Evaluate for parasitized red blood cells.
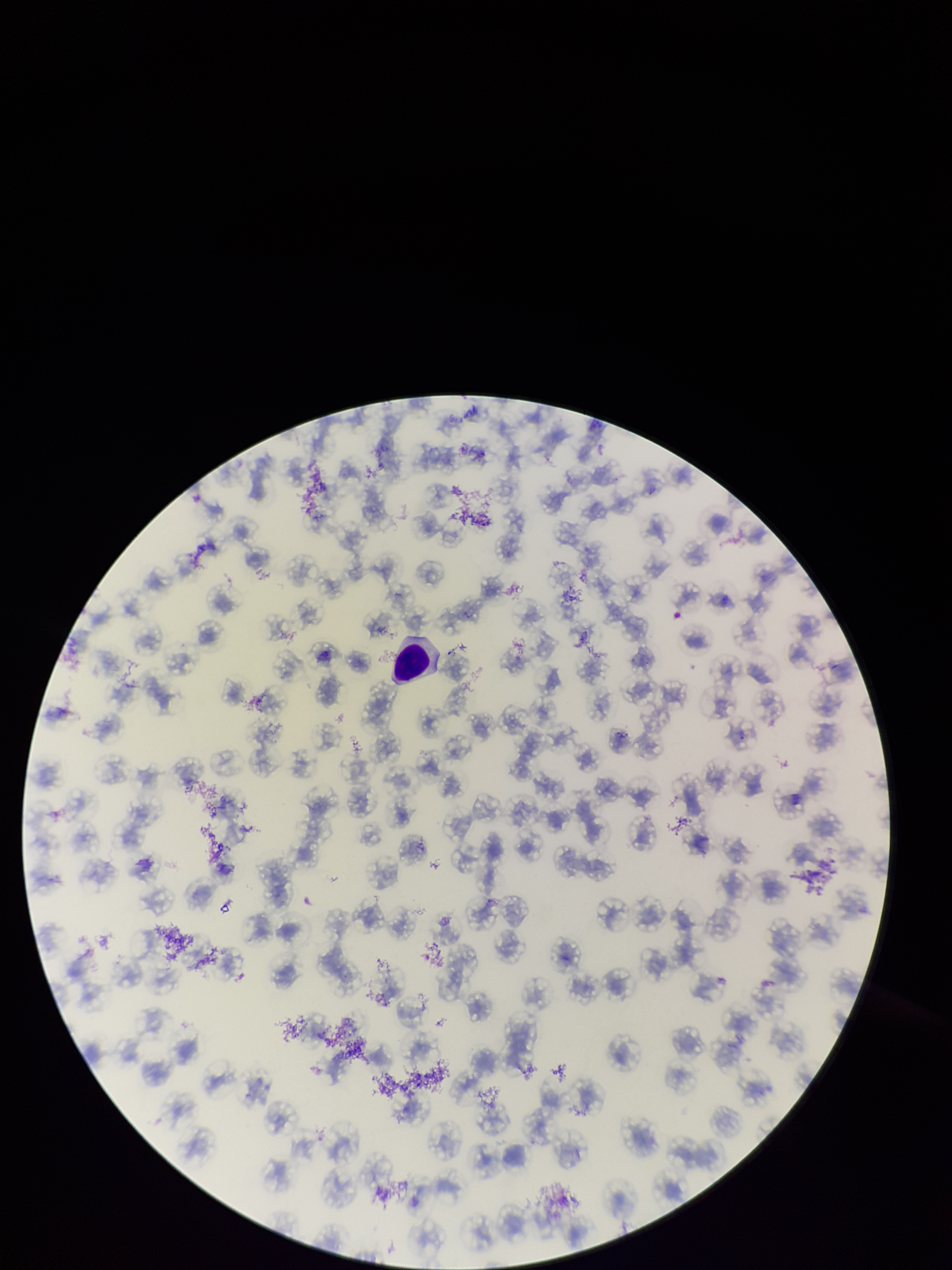

None identified.

Smartphone photograph taken through the eyepiece of a microscope. One field from this slide. Parasitized red blood cell count: 0. Species reported for this patient: Plasmodium falciparum. Red blood cell count: 99. Giemsa stain. Image is 952×1270 pixels. Preparation: thin. Patient malaria status: positive.